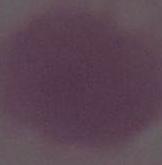
An erythrocyte is seen. Captured at 1000x magnification. Micrograph.